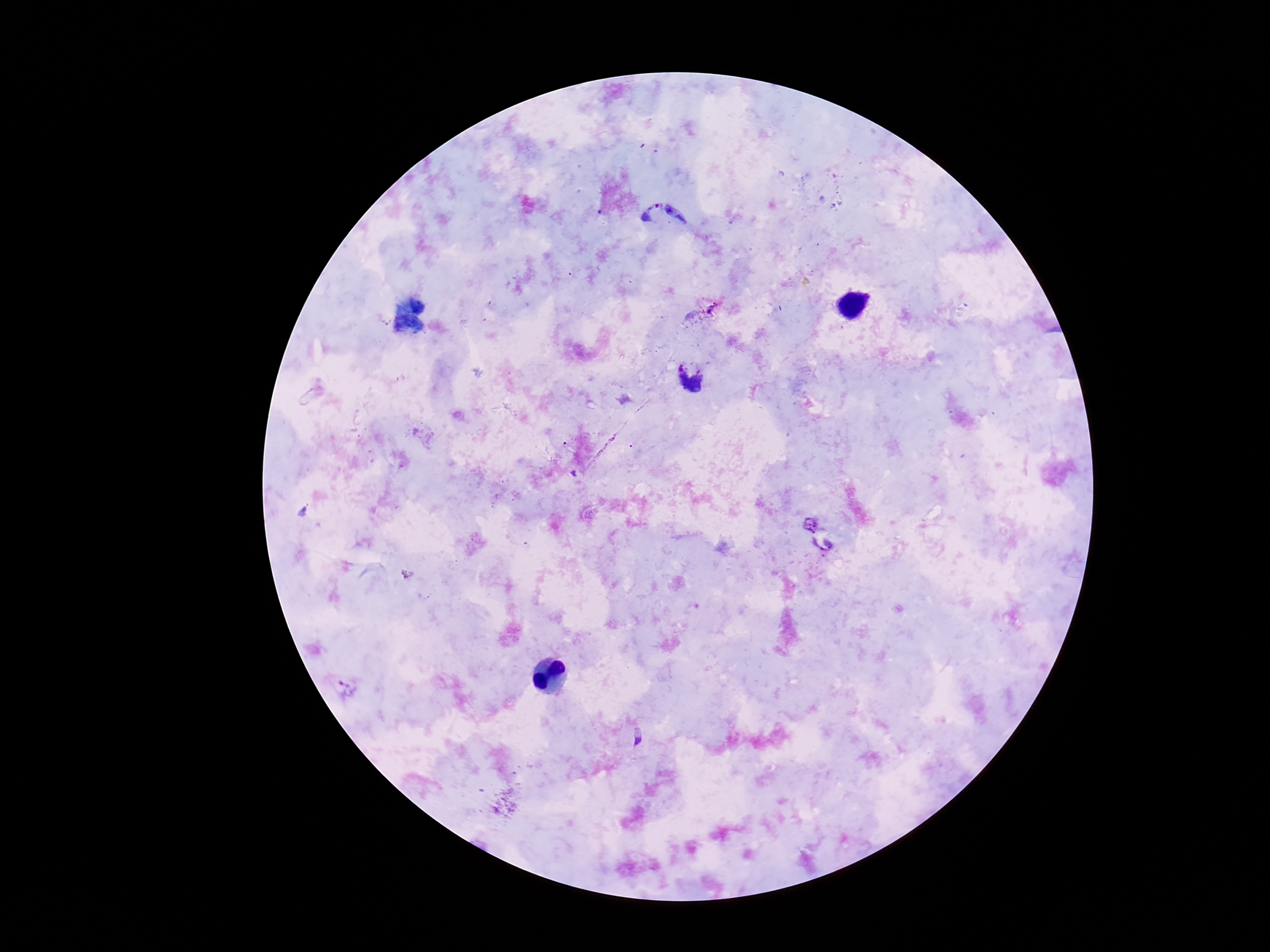

stain = Giemsa
patient malaria status = positive
image size = 1270×952 pixels
field of view = single
capture = smartphone camera through the microscope eyepiece
magnification = 100x
preparation = thick peripheral-blood smear
Plasmodium parasite locations = approximate centers as {x, y} in pixels: {663, 223}, {690, 376}, {348, 688}